Name the parasite shown.
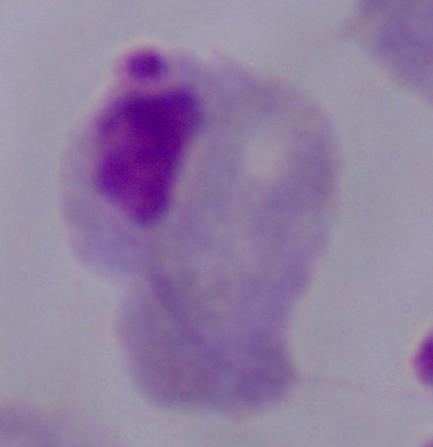

This is a trichomonad.

Summary:
  - Modality: photomicrograph
  - Magnification: 1000x